Name the parasite shown.
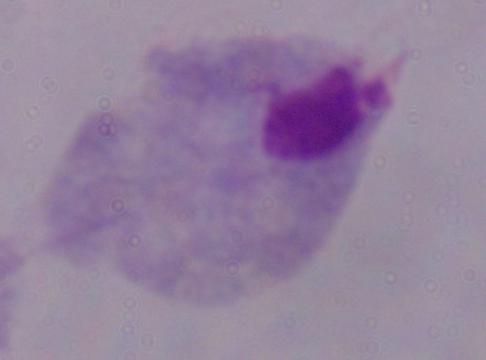
This is a trichomonad.

modality: micrograph
magnification: 1000x